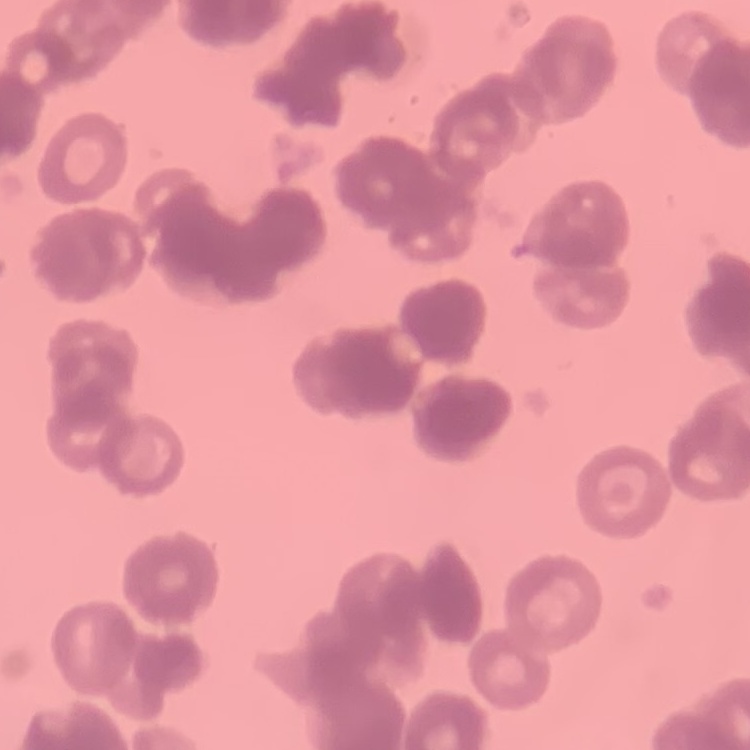

Summary:
  - Red blood cell morphology: rouleaux formation
  - Image type: square crop of a larger photomicrograph
  - Preparation: thin peripheral smear
  - Stain: Field's or Giemsa